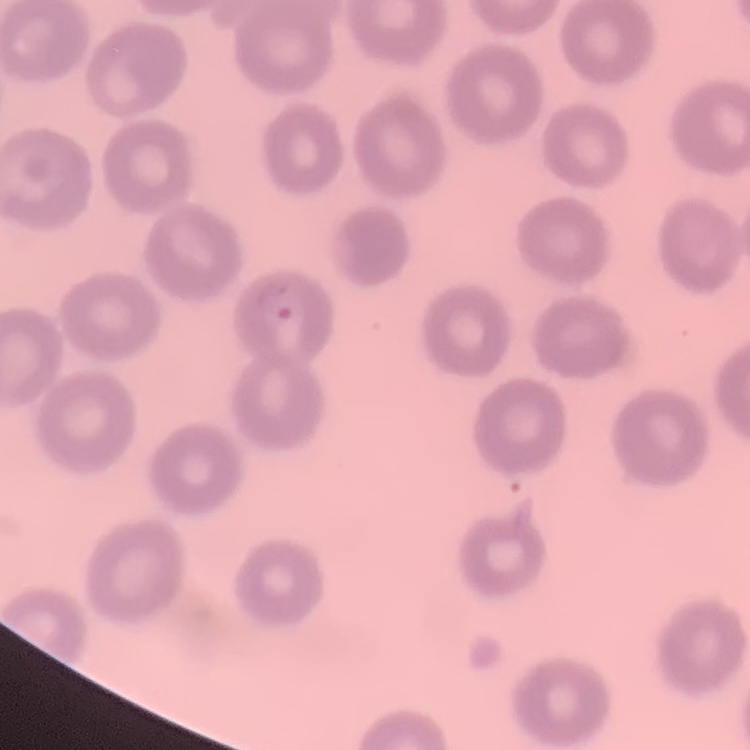

{
  "erythrocyte_morphology": "no rouleaux formation",
  "preparation": "thin peripheral smear",
  "image_type": "one tile cut from a larger photomicrograph",
  "stain": "Field's or Giemsa"
}